Give the position of every leukocyte.
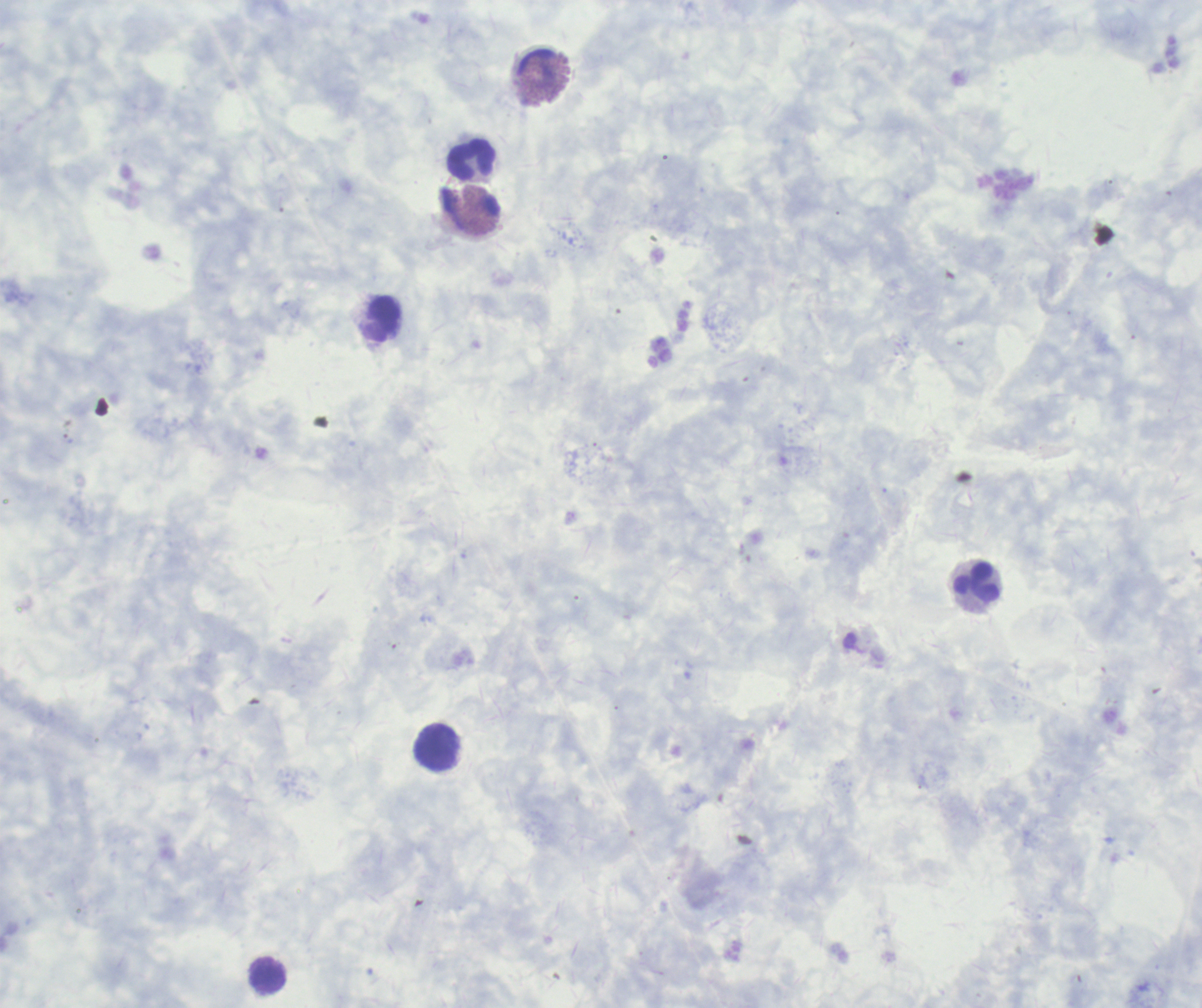
Approximate centers as [x, y] in pixels.
Leukocytes: [472, 159], [382, 319], [976, 582], [436, 748], [268, 976].

stain = Romanowsky
context = previously used in an actual diagnosis
background quality = unsatisfactory
preparation = thick smear of blood
magnification = 100x
result = negative for Plasmodium parasites
field of view = one from this slide
image size = 1202×1008 pixels
coloration quality = good